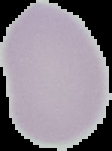
Summary:
  - Preparation: thin blood film
  - Image size: 112×151 pixels
  - Result: no malaria parasites detected
  - Image type: cell region segmented out of the field of view; surrounding area masked to black